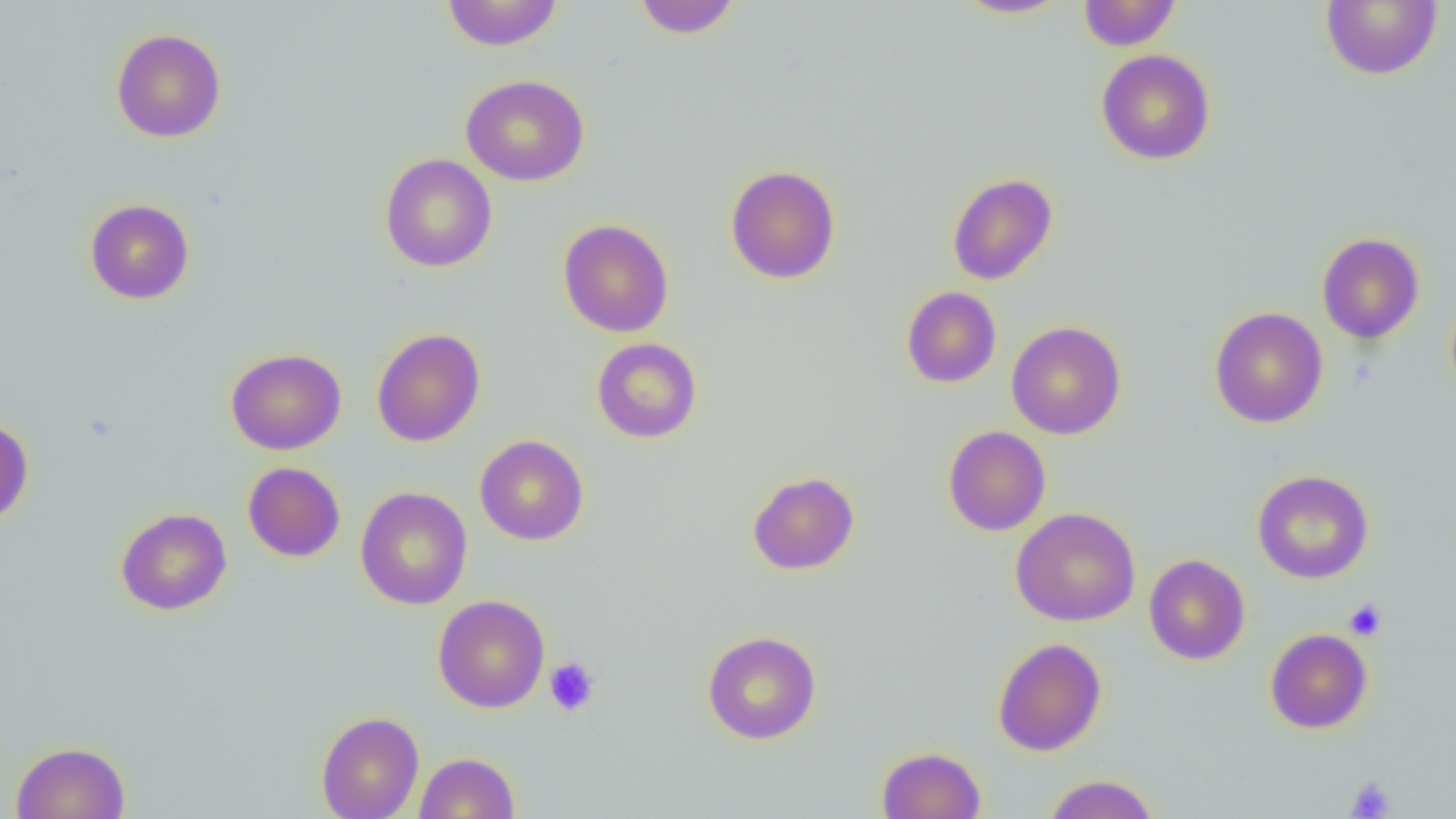

Approximate bounding boxes as named x1/y1/x2/y2 corners in pixels. Platelet locations: (x1=1344, y1=598, x2=1387, y2=641), (x1=544, y1=657, x2=601, y2=717), (x1=1345, y1=776, x2=1396, y2=818). Uninfected red blood cell locations: (x1=441, y1=0, x2=564, y2=51), (x1=630, y1=0, x2=743, y2=39), (x1=954, y1=0, x2=1069, y2=19), (x1=1077, y1=0, x2=1182, y2=51), (x1=1321, y1=0, x2=1443, y2=80), (x1=111, y1=28, x2=226, y2=143), (x1=1096, y1=49, x2=1216, y2=165), (x1=460, y1=74, x2=590, y2=187), (x1=379, y1=153, x2=497, y2=272), (x1=724, y1=164, x2=841, y2=285), (x1=947, y1=173, x2=1058, y2=285), (x1=85, y1=199, x2=194, y2=304), (x1=558, y1=218, x2=674, y2=337), (x1=1316, y1=232, x2=1425, y2=344), (x1=901, y1=286, x2=1001, y2=388), (x1=1210, y1=306, x2=1328, y2=428), (x1=1006, y1=321, x2=1126, y2=440), (x1=371, y1=327, x2=485, y2=447), (x1=591, y1=337, x2=702, y2=443), (x1=225, y1=348, x2=346, y2=455), (x1=0, y1=417, x2=34, y2=527), (x1=943, y1=425, x2=1051, y2=536), (x1=474, y1=434, x2=589, y2=546), (x1=242, y1=461, x2=345, y2=562), (x1=1252, y1=469, x2=1374, y2=584), (x1=747, y1=471, x2=860, y2=575), (x1=355, y1=487, x2=472, y2=609), (x1=1011, y1=507, x2=1141, y2=627), (x1=115, y1=508, x2=232, y2=615), (x1=1144, y1=554, x2=1250, y2=665), (x1=432, y1=594, x2=550, y2=713), (x1=1265, y1=628, x2=1373, y2=734), (x1=702, y1=630, x2=821, y2=744), (x1=993, y1=638, x2=1107, y2=756), (x1=316, y1=711, x2=424, y2=819), (x1=10, y1=741, x2=131, y2=819), (x1=876, y1=746, x2=986, y2=818), (x1=415, y1=752, x2=520, y2=818), (x1=1044, y1=773, x2=1159, y2=819). Slide-level diagnosis: negative for blood parasites. Optical microscopy. Image is 1456×819 pixels. Thin blood smear. 1000x magnification. Single field of view.